Comment on the morphology of the erythrocytes.
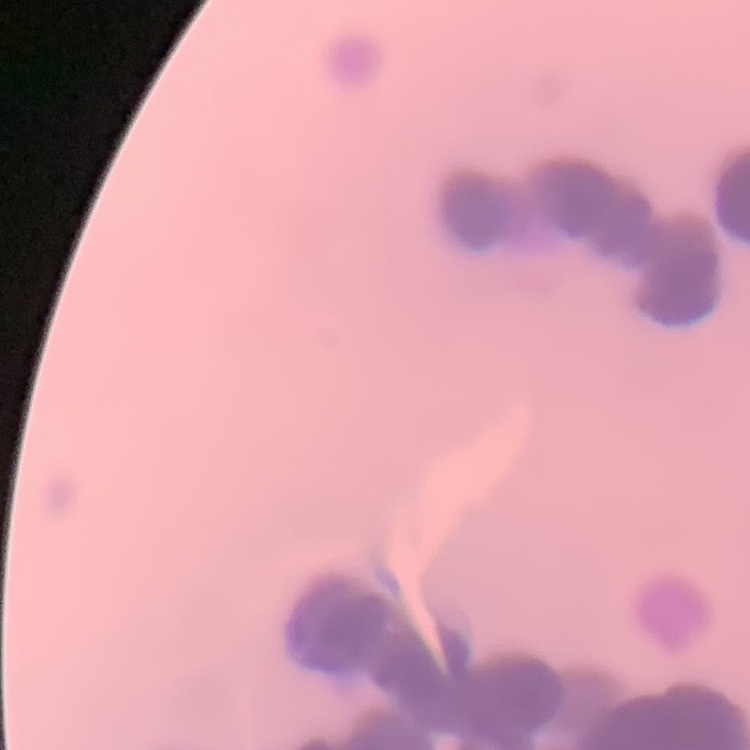
They show rouleaux formation.

Thin blood film. Field's or Giemsa stain. Square crop of a larger photomicrograph.